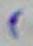

magnification: 1000x
identification: Toxoplasma gondii
modality: photomicrograph